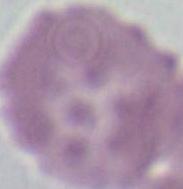 Micrograph. Captured at 1000x magnification. A red blood cell is seen.